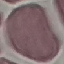
Summary:
  - Result: no malaria parasites detected
  - Stain: Giemsa
  - Capture: smartphone camera at the microscope eyepiece
  - Preparation: thin blood film
  - Image type: automatically extracted cell patch, resized to 64 × 64 pixels